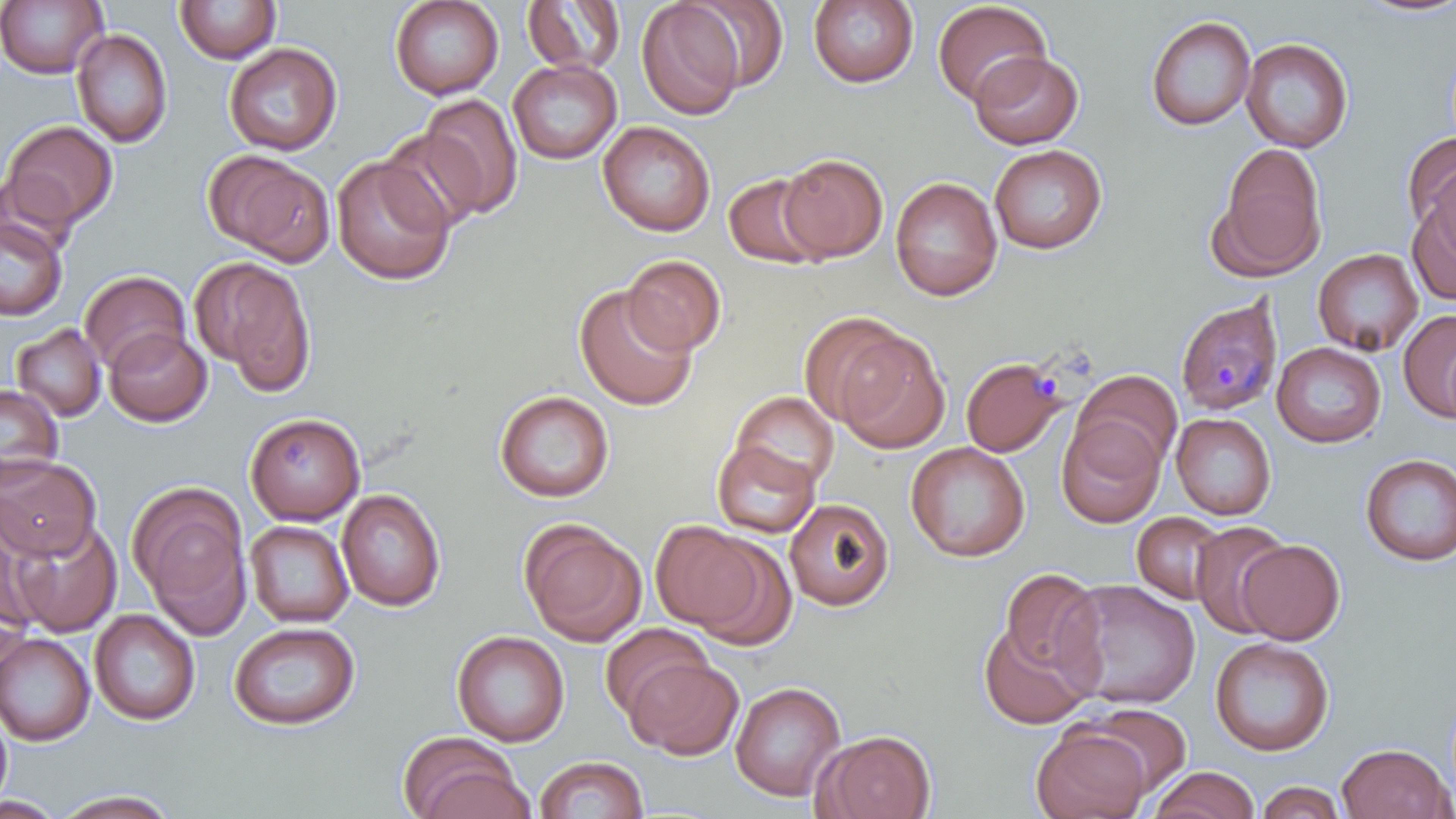

Summary:
  - Coordinate format: approximate bounding boxes as named x1/y1/x2/y2 corners in pixels
  - Plasmodium malariae-infected red blood cell locations: (x1=1175, y1=296, x2=1283, y2=417), (x1=959, y1=358, x2=1063, y2=457)
  - Uninfected red blood cell locations: (x1=0, y1=0, x2=108, y2=79), (x1=390, y1=0, x2=503, y2=100), (x1=685, y1=0, x2=789, y2=92), (x1=1352, y1=0, x2=1456, y2=19), (x1=174, y1=1, x2=281, y2=64), (x1=523, y1=1, x2=626, y2=75), (x1=807, y1=1, x2=918, y2=88), (x1=932, y1=1, x2=1052, y2=107), (x1=637, y1=2, x2=745, y2=120), (x1=1145, y1=15, x2=1255, y2=131), (x1=72, y1=28, x2=173, y2=148), (x1=1240, y1=37, x2=1354, y2=153), (x1=224, y1=43, x2=342, y2=156), (x1=969, y1=51, x2=1084, y2=149), (x1=508, y1=59, x2=621, y2=164), (x1=419, y1=94, x2=524, y2=219), (x1=1, y1=120, x2=118, y2=229), (x1=598, y1=121, x2=715, y2=236), (x1=380, y1=129, x2=486, y2=232), (x1=1401, y1=133, x2=1456, y2=240), (x1=1210, y1=142, x2=1328, y2=281), (x1=989, y1=144, x2=1107, y2=254), (x1=205, y1=151, x2=335, y2=266), (x1=777, y1=154, x2=889, y2=262), (x1=331, y1=155, x2=454, y2=286), (x1=723, y1=171, x2=829, y2=269), (x1=889, y1=177, x2=1003, y2=302), (x1=1406, y1=195, x2=1456, y2=306), (x1=0, y1=215, x2=67, y2=321), (x1=1313, y1=247, x2=1423, y2=357), (x1=622, y1=254, x2=726, y2=355), (x1=190, y1=256, x2=317, y2=393), (x1=80, y1=270, x2=190, y2=374), (x1=574, y1=285, x2=698, y2=411), (x1=1398, y1=309, x2=1456, y2=423), (x1=797, y1=311, x2=910, y2=426), (x1=11, y1=323, x2=106, y2=421), (x1=104, y1=328, x2=211, y2=426), (x1=835, y1=331, x2=951, y2=454), (x1=1271, y1=342, x2=1385, y2=448), (x1=1073, y1=370, x2=1183, y2=472), (x1=0, y1=383, x2=63, y2=485), (x1=494, y1=390, x2=614, y2=502), (x1=730, y1=391, x2=839, y2=492), (x1=244, y1=412, x2=366, y2=524), (x1=1171, y1=412, x2=1276, y2=520), (x1=1056, y1=414, x2=1166, y2=528), (x1=711, y1=440, x2=820, y2=538), (x1=905, y1=441, x2=1030, y2=562), (x1=0, y1=453, x2=100, y2=561), (x1=1359, y1=453, x2=1456, y2=566), (x1=126, y1=480, x2=250, y2=629), (x1=337, y1=488, x2=446, y2=611), (x1=784, y1=498, x2=895, y2=611), (x1=1132, y1=512, x2=1227, y2=603), (x1=6, y1=517, x2=122, y2=638), (x1=0, y1=518, x2=46, y2=641), (x1=519, y1=518, x2=646, y2=646), (x1=1190, y1=519, x2=1292, y2=638), (x1=244, y1=520, x2=354, y2=627), (x1=650, y1=521, x2=767, y2=632), (x1=685, y1=534, x2=797, y2=650), (x1=1237, y1=540, x2=1345, y2=645), (x1=998, y1=567, x2=1105, y2=682), (x1=1057, y1=578, x2=1201, y2=710), (x1=90, y1=609, x2=200, y2=726), (x1=978, y1=616, x2=1099, y2=729), (x1=228, y1=621, x2=360, y2=730), (x1=600, y1=623, x2=712, y2=720), (x1=452, y1=630, x2=569, y2=747), (x1=0, y1=633, x2=95, y2=746), (x1=1209, y1=637, x2=1334, y2=756), (x1=624, y1=656, x2=743, y2=760), (x1=730, y1=681, x2=846, y2=801), (x1=1079, y1=702, x2=1192, y2=798), (x1=0, y1=710, x2=13, y2=811), (x1=1031, y1=725, x2=1152, y2=819), (x1=815, y1=729, x2=937, y2=819), (x1=397, y1=732, x2=530, y2=819), (x1=1336, y1=742, x2=1454, y2=819), (x1=534, y1=755, x2=648, y2=818), (x1=1147, y1=766, x2=1259, y2=818), (x1=1255, y1=781, x2=1347, y2=819), (x1=51, y1=789, x2=181, y2=817), (x1=0, y1=795, x2=66, y2=819)
  - Slide-level diagnosis: Plasmodium malariae
  - Field of view: single
  - Preparation: thin blood film
  - Modality: light microscopy
  - Image size: 1456×819 pixels
  - Stain: May-Grünwald-Giemsa
  - Magnification: 1000x